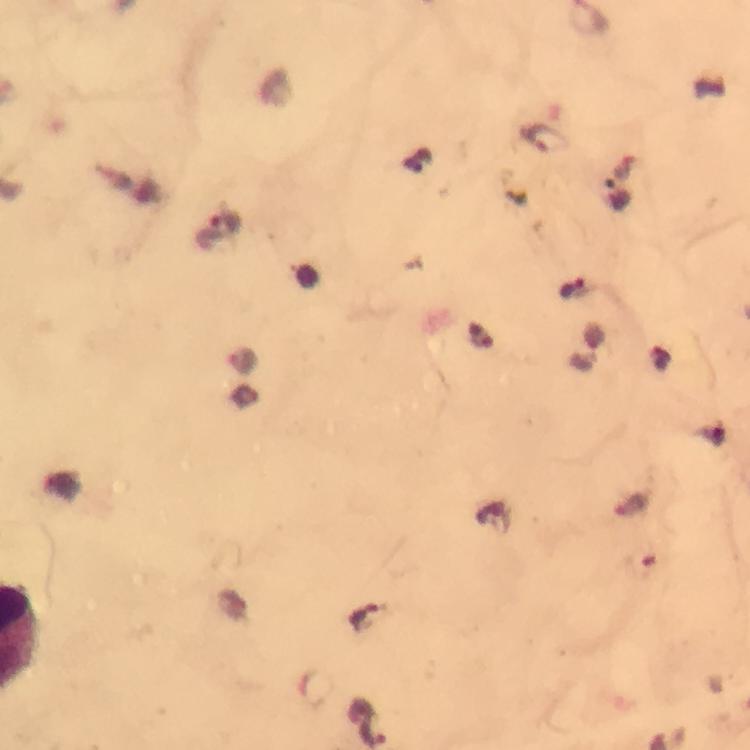

magnification: 100x
plasmodium_parasite_locations: 'approximate centers as (x, y) in pixels: (545, 138), (220, 226), (574, 289), (482, 334), (242, 360)'
context: from a malaria diagnostic workup
capture: smartphone mounted on the microscope
immersion_oil: used
stain: Giemsa
image_size: 750×750 pixels
preparation: thick blood smear
cropped_from: a single field of view